Describe the morphology of the erythrocytes.
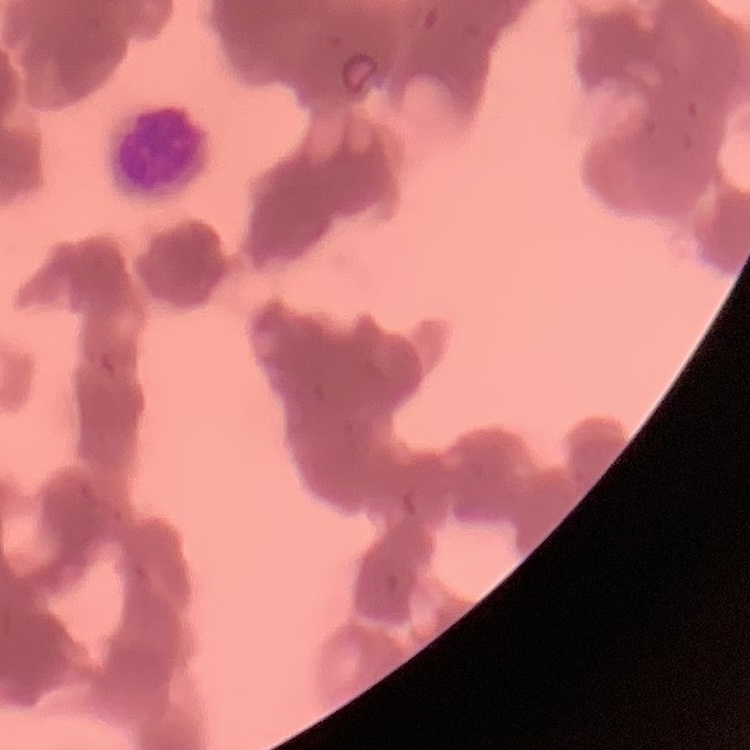
Rouleaux formation.

Summary:
  - Image type: square crop of a larger photomicrograph
  - Preparation: thin peripheral smear
  - Stain: Field's or Giemsa